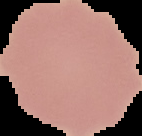 Segmented cell region on a black background. Result: no Plasmodium parasites detected. From a thin blood film. Image is 142×136 pixels.